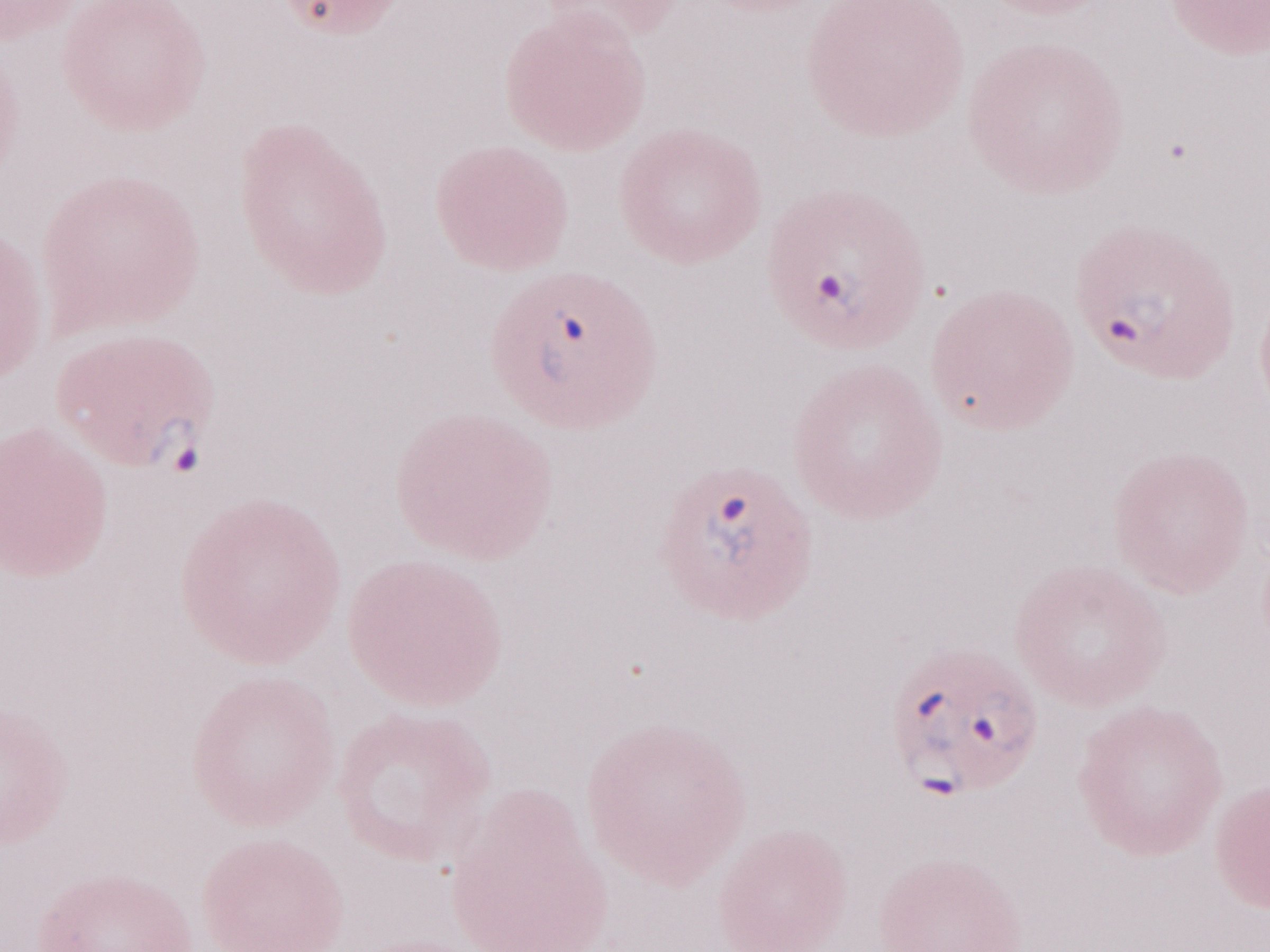
Image is 1270×952 pixels. Thin blood film. Malaria diagnosis (patient-level): positive. One field of this slide. 1,000x magnification. Olympus BX43 microscope, Olympus DP73 camera. May-Grünwald-Giemsa stain.